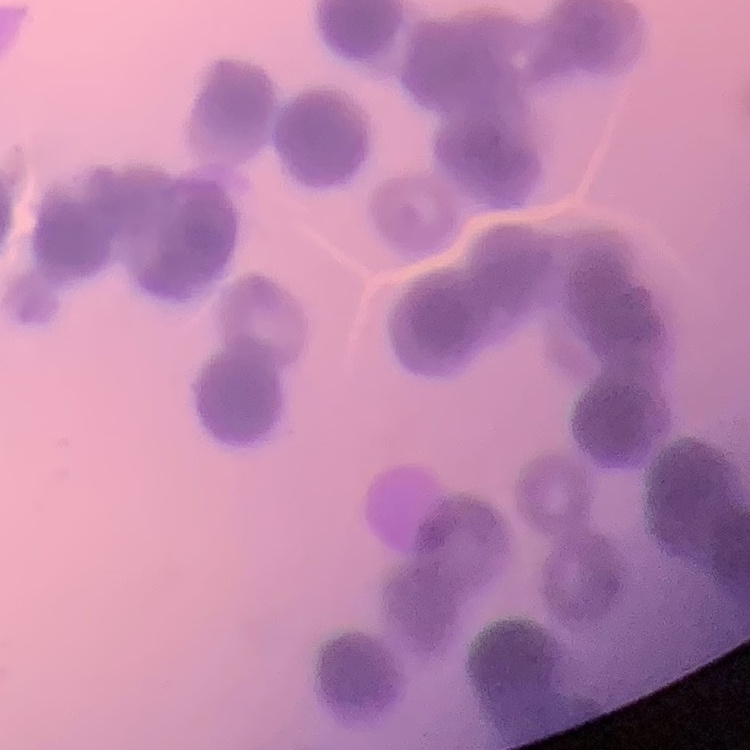

Summary:
  - Erythrocyte morphology: rouleaux formation
  - Image type: one tile cut from a larger photomicrograph
  - Preparation: thin blood film
  - Stain: Field's or Giemsa